Classify this cell by malaria status.
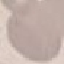
It is uninfected.

Acquired by smartphone through the microscope eyepiece. Thin blood film. Automatically extracted cell patch, resized to 64 × 64 pixels. Giemsa stain.